State which parasite is depicted.
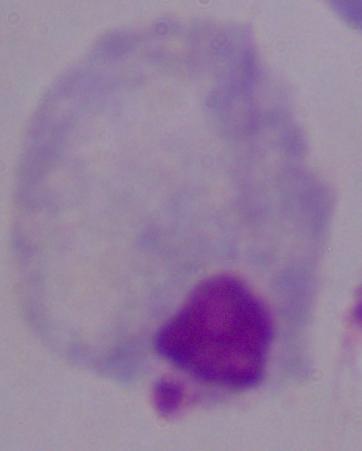
A trichomonad.

Summary:
  - Magnification: 1000x
  - Modality: micrograph